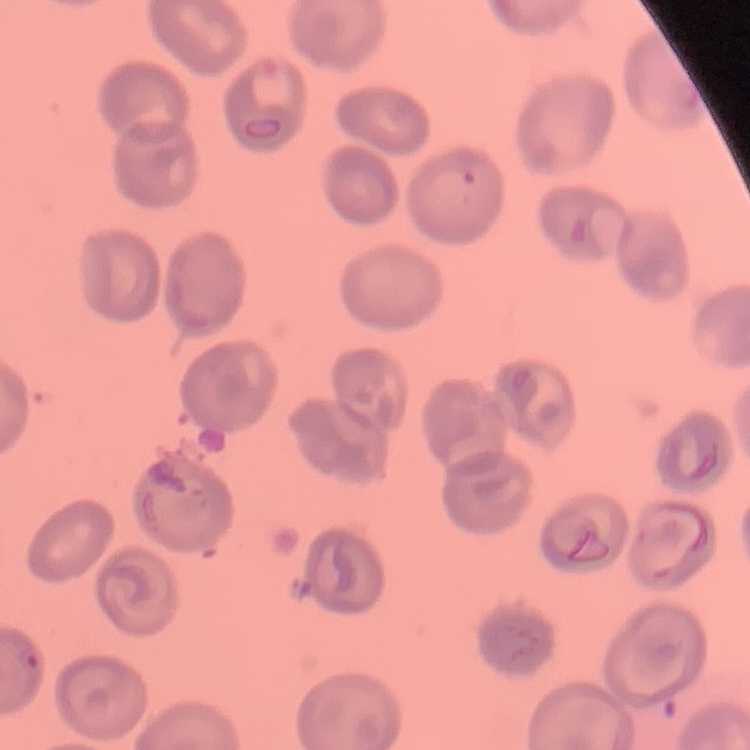

Summary:
  - Erythrocyte morphology: no rouleaux formation
  - Preparation: thin blood film
  - Stain: Field's or Giemsa
  - Image type: one tile cut from a larger photomicrograph